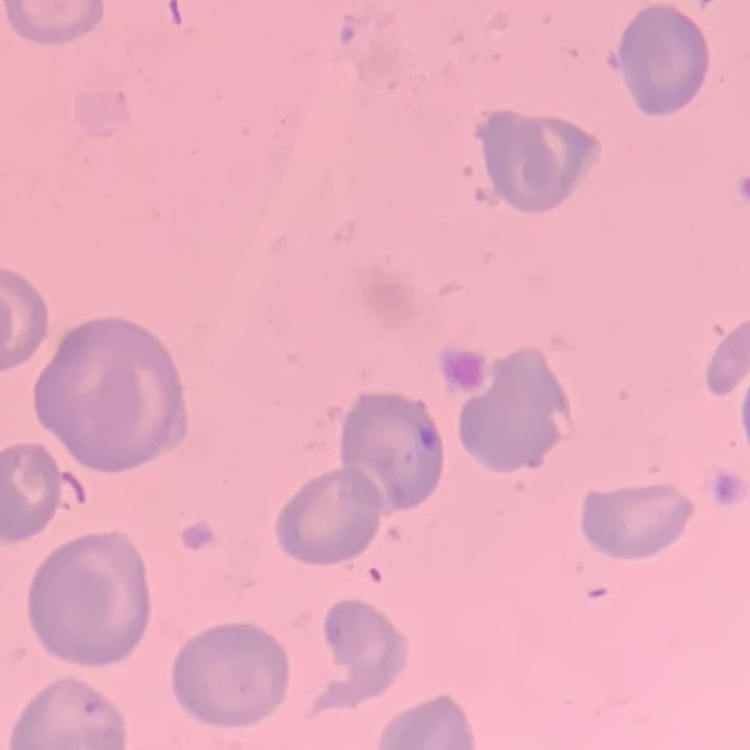 The erythrocytes show no rouleaux formation. Square crop of a larger photomicrograph. Thin blood film. Field's or Giemsa stain.